Name the cell type shown.
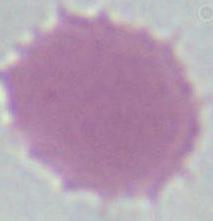
An erythrocyte.

magnification = 1000x
modality = micrograph